Locate every Plasmodium parasite.
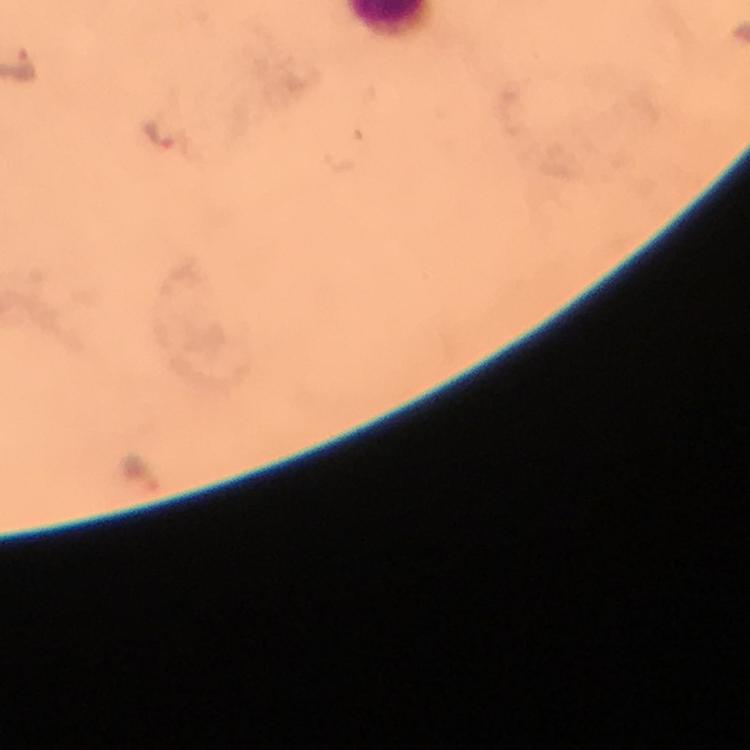

Approximate centers as (x, y) in pixels.
Plasmodium parasites: (17, 64), (158, 133).

Summary:
  - Capture: smartphone photograph through a microscope
  - Image size: 750×750 pixels
  - Immersion oil: applied
  - Cropped from: one field of view
  - Magnification: 100x
  - Preparation: thick blood film
  - Context: from a diagnostic examination for malaria
  - Stain: Giemsa